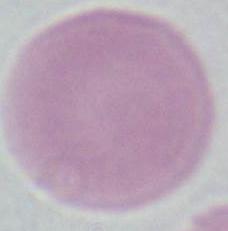
Summary:
  - Magnification: 1000x
  - Modality: photomicrograph
  - Identification: erythrocyte